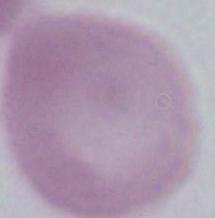
magnification = 1000x
identification = red blood cell
modality = photomicrograph